Locate every blood parasite and identify its species.
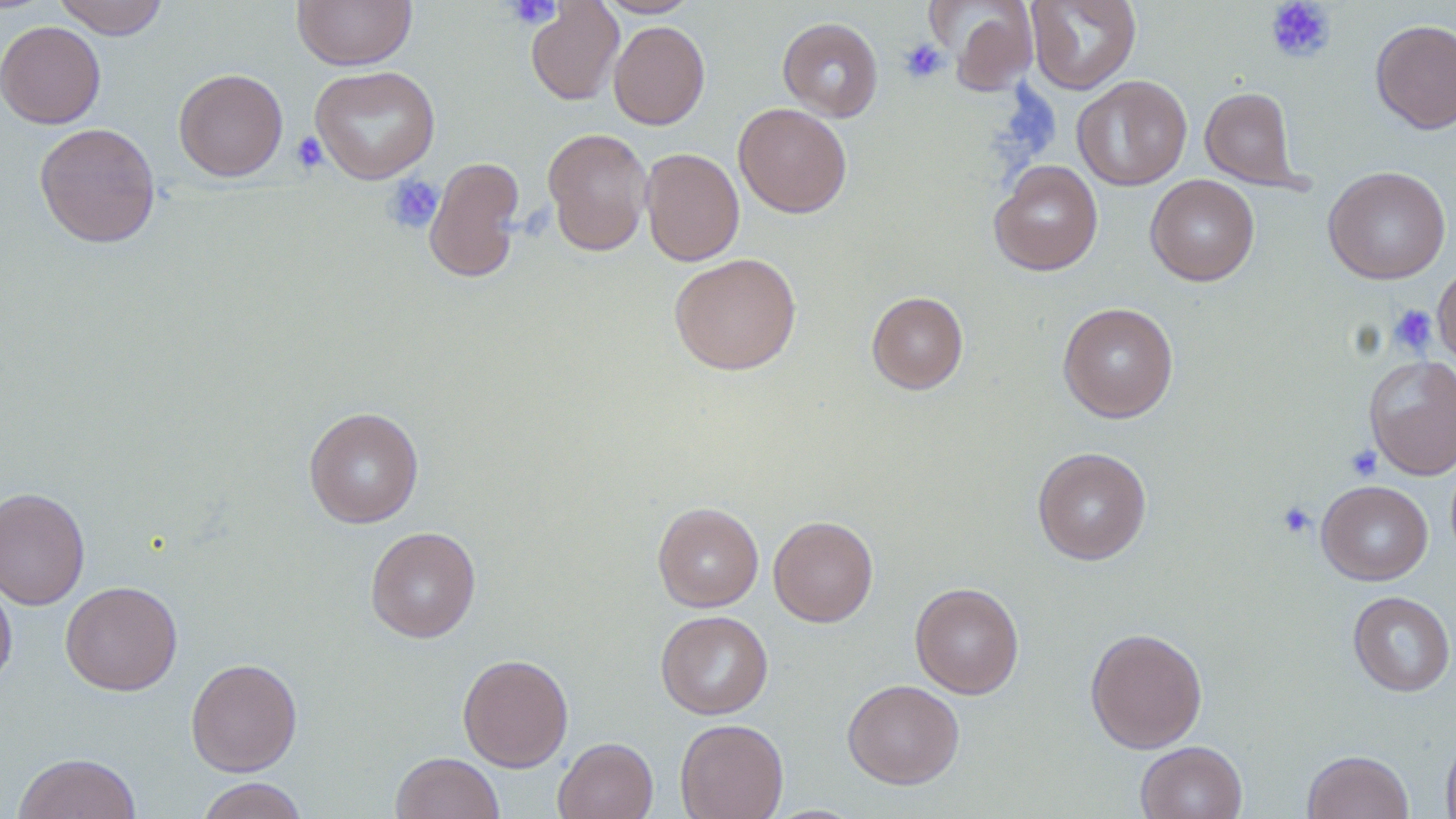
No blood parasites observed.

Approximate bounding boxes as (x1,y1)-(x2,y2) corner pairs in pixels. Uninfected red blood cell locations: (53,0)-(169,39), (292,0)-(416,70), (596,0)-(700,18), (1026,0)-(1141,94), (526,1)-(624,106), (932,1)-(1039,95), (778,17)-(883,122), (1370,19)-(1456,134), (0,21)-(106,129), (608,21)-(710,129), (310,65)-(440,184), (173,68)-(288,182), (1072,75)-(1192,191), (1200,86)-(1303,189), (734,102)-(852,218), (34,122)-(161,248), (542,127)-(653,256), (641,148)-(744,266), (424,156)-(526,283), (989,160)-(1103,276), (1323,166)-(1450,284), (1145,174)-(1260,286), (669,252)-(802,375), (1433,261)-(1456,370), (867,291)-(968,394), (1058,302)-(1179,423), (1364,354)-(1456,479), (303,406)-(424,528), (1032,446)-(1151,565), (1317,480)-(1432,585), (0,486)-(91,610), (653,502)-(764,611), (768,515)-(878,627), (365,526)-(481,642), (0,574)-(16,691), (60,580)-(183,696), (910,581)-(1024,698), (1347,590)-(1455,696), (655,610)-(773,719), (1085,627)-(1207,753), (457,653)-(574,771), (186,658)-(303,777), (843,679)-(965,789), (675,718)-(788,819), (1441,733)-(1456,819), (553,737)-(658,819), (1135,741)-(1247,819), (1303,750)-(1414,819), (12,752)-(142,818), (391,752)-(504,819), (196,777)-(309,819). Platelet locations: (504,0)-(564,28), (1265,0)-(1336,62), (899,40)-(948,83), (291,131)-(328,174), (383,173)-(445,234), (1387,304)-(1436,357), (1345,444)-(1383,482), (1277,501)-(1317,539). Slide-level diagnosis: no evidence of blood parasites. One field of a larger specimen. Captured at 1000x magnification. Light microscopy. Image is 1456×819 pixels. Thin blood smear. May-Grünwald-Giemsa stain.